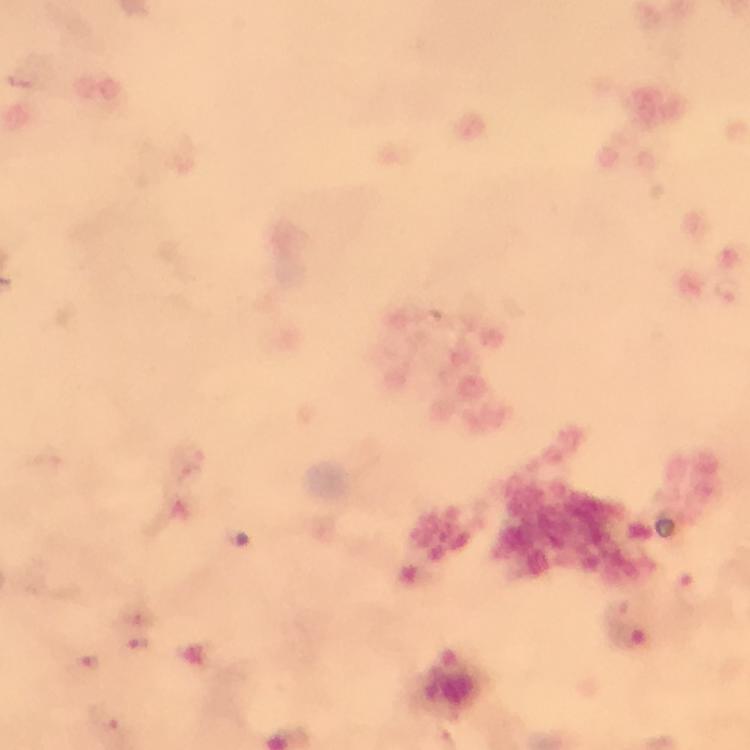
Approximate centers as {x, y} in pixels.
Summary:
  - Malaria parasite locations: {726, 289}, {617, 613}, {139, 645}, {87, 660}
  - Magnification: 100x
  - Cropped from: a single field of view
  - Capture: smartphone mounted on the microscope
  - Image size: 750×750 pixels
  - Preparation: thick smear
  - Context: from a malaria diagnostic workup
  - Immersion oil: applied
  - Stain: Giemsa